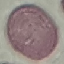
Summary:
  - Malaria status: uninfected
  - Capture: smartphone camera at the microscope eyepiece
  - Preparation: thin smear
  - Image type: cell patch, automatically extracted from a larger field of view and resized to 64 × 64 pixels
  - Stain: Giemsa